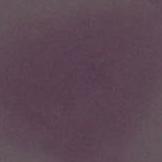

Captured at 1000x magnification. Micrograph. A red blood cell is seen.